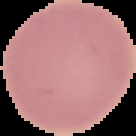
Summary:
  - Result: no malaria parasites seen
  - Image size: 136×136 pixels
  - Preparation: thin blood smear
  - Image type: segmented cell region on a black background